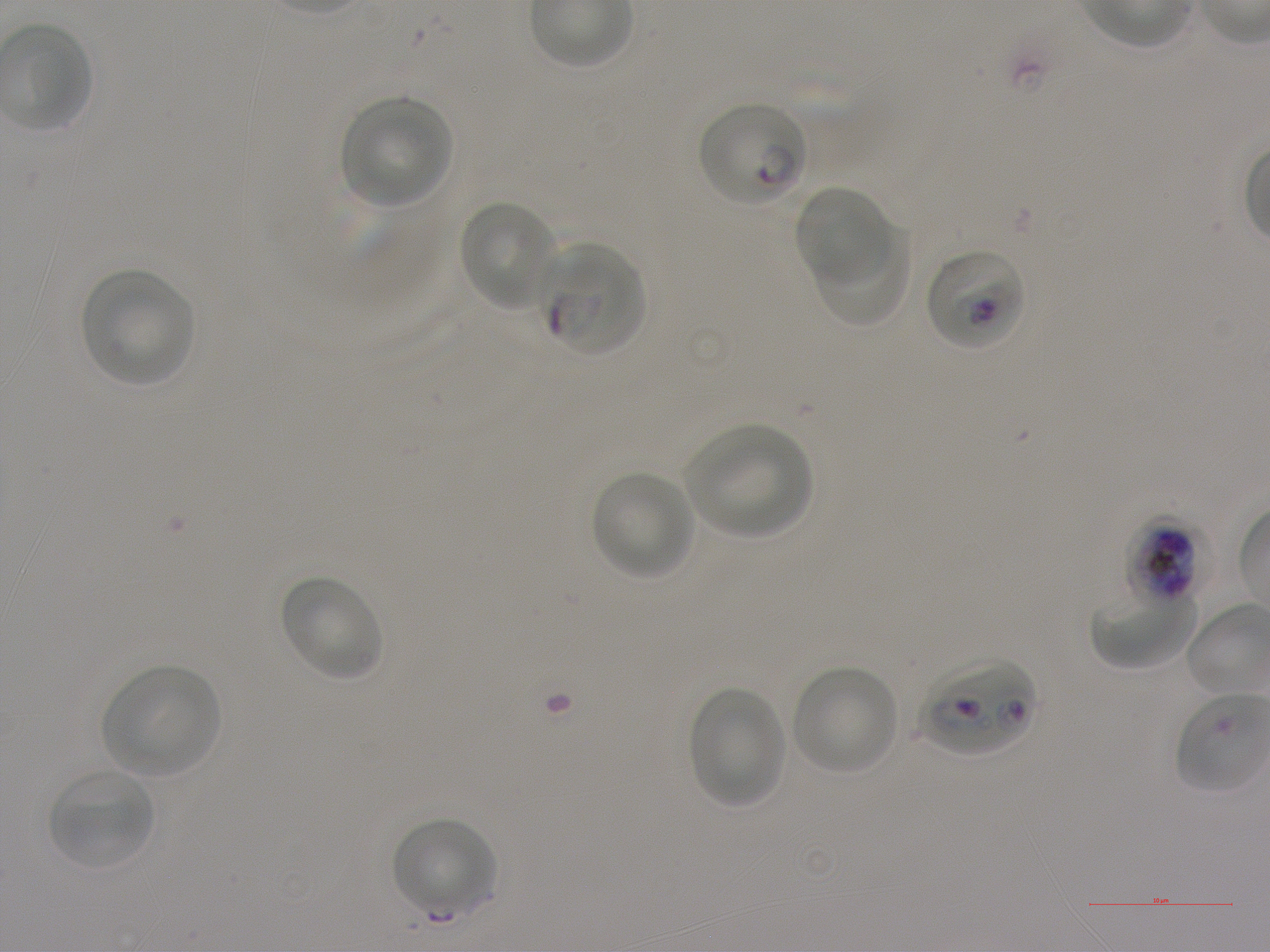

Not every red blood cell is marked. A life-cycle stage — or a range of stages, where the recorded stages span more than one — follows each staged infected red blood cell.
objective: 100x, oil immersion, numerical aperture 1.25
locations_of_infected_red_blood_cells: 'approximate bounding boxes as {x1, y1, x2, y2} in pixels: {698, 103, 807, 207} ring; {542, 243, 645, 357} early ring to early trophozoite; {926, 250, 1026, 351} late ring to late trophozoite; {1125, 518, 1213, 604} late trophozoite to early schizont; {919, 656, 1036, 756}'
locations_of_uninfected_red_blood_cells: 'approximate bounding boxes as {x1, y1, x2, y2} in pixels: {2, 25, 90, 130}, {339, 96, 451, 207}, {792, 185, 891, 286}, {458, 200, 557, 311}, {816, 228, 911, 330}, {79, 266, 193, 388}, {682, 422, 812, 540}, {591, 470, 694, 581}, {279, 575, 385, 682}, {1090, 589, 1198, 670}, {102, 666, 221, 777}, {792, 666, 899, 774}, {689, 686, 787, 809}, {48, 769, 155, 868}, {391, 817, 499, 918}'
image_size: 1270×952 pixels
stain: Giemsa
preparation: thin blood smear
locations_of_red_blood_cells_of_indeterminate_infection_status: 'approximate bounding boxes as {x1, y1, x2, y2} in pixels: {1173, 693, 1268, 794}'
field_of_view: one from this slide
culture: in-vitro Plasmodium falciparum strain NF54, static
donor_blood_group: A+